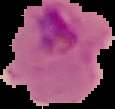
image type = segmented cell region on a black background
result = Plasmodium parasites identified
preparation = thin blood smear
image size = 115×109 pixels